Comment on the morphology of the erythrocytes.
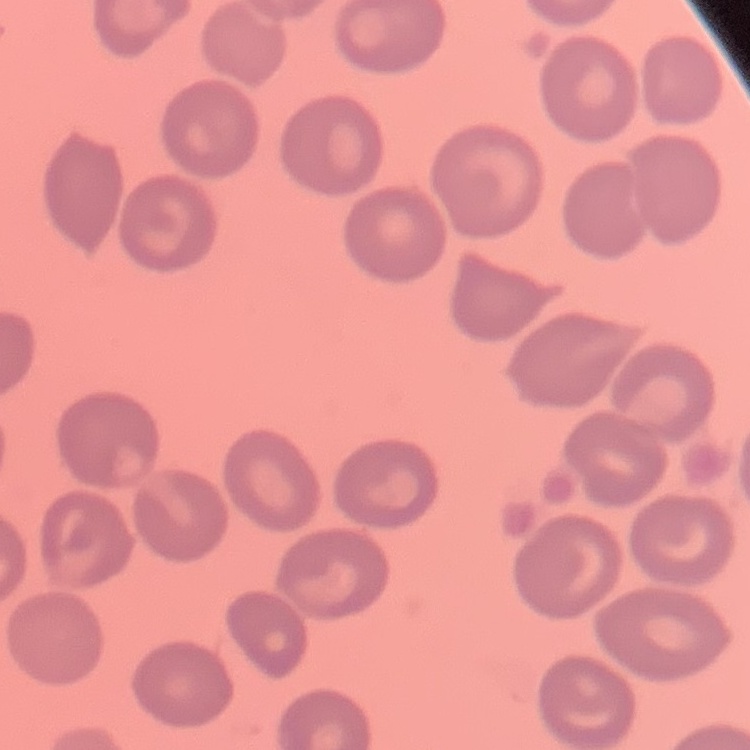

No rouleaux formation.

{
  "image_type": "square crop of a larger photomicrograph",
  "preparation": "thin peripheral smear",
  "stain": "Field's or Giemsa"
}